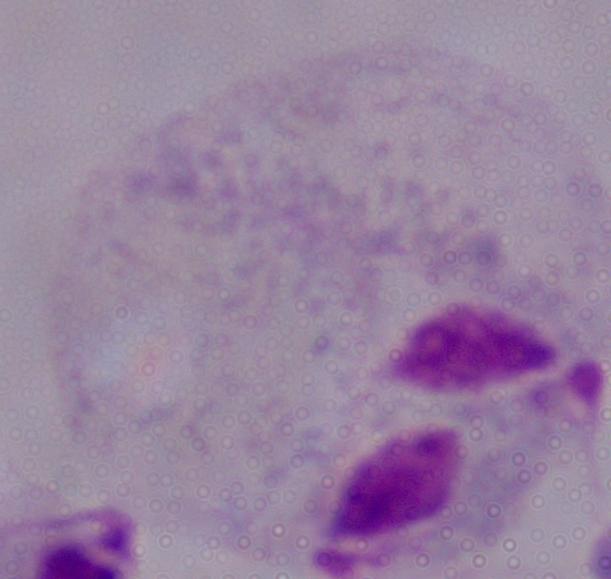
Captured at 1000x magnification. A trichomonad is shown. Photomicrograph.